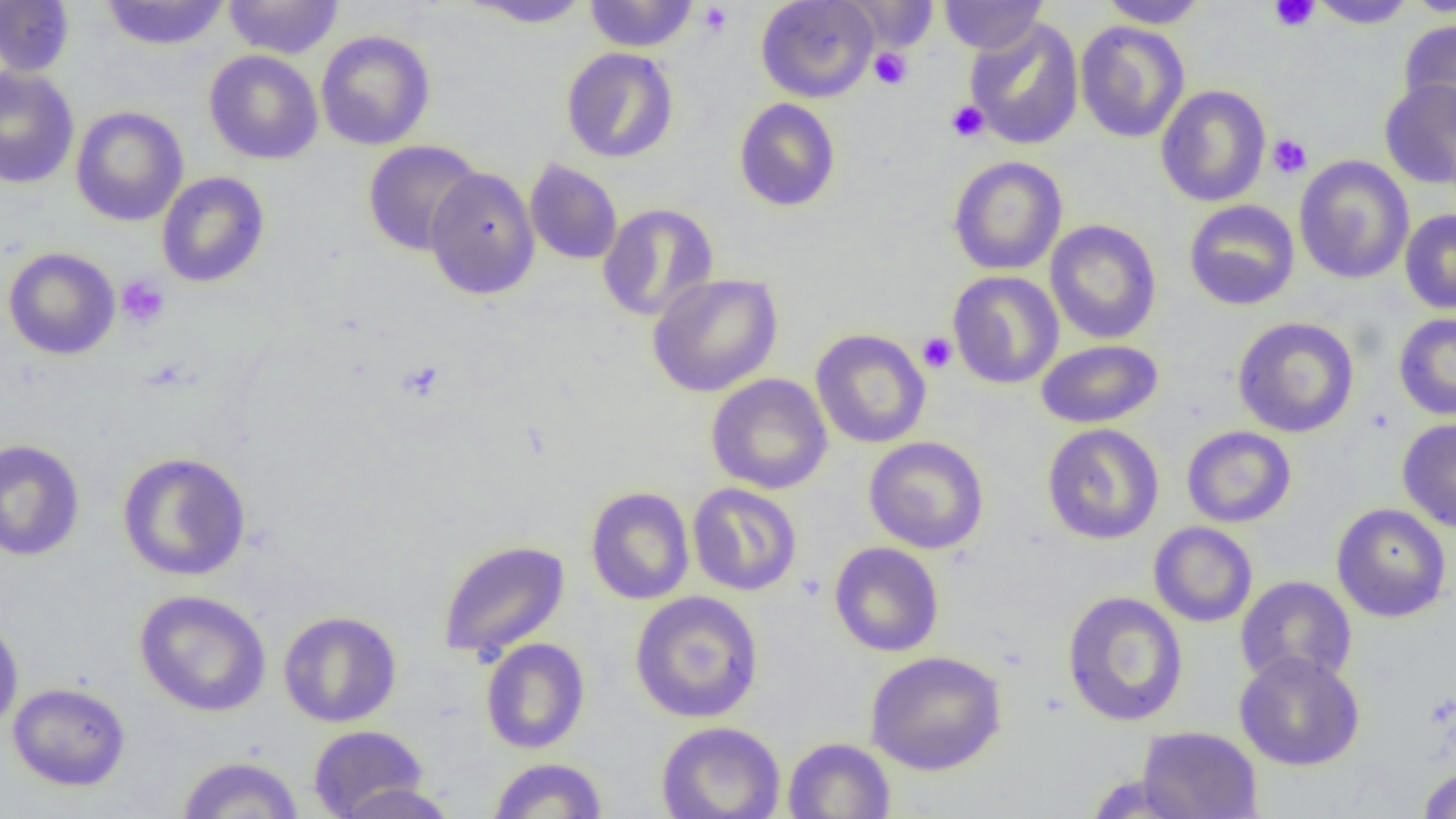 Approximate bounding boxes as named x1/y1/x2/y2 corners in pixels. Uninfected red blood cell locations: (x1=223, y1=0, x2=343, y2=59), (x1=461, y1=0, x2=594, y2=29), (x1=584, y1=0, x2=699, y2=52), (x1=756, y1=0, x2=879, y2=103), (x1=841, y1=0, x2=939, y2=51), (x1=939, y1=0, x2=1048, y2=55), (x1=1097, y1=0, x2=1209, y2=28), (x1=1309, y1=0, x2=1417, y2=29), (x1=1400, y1=0, x2=1456, y2=17), (x1=0, y1=1, x2=75, y2=78), (x1=99, y1=1, x2=231, y2=50), (x1=964, y1=17, x2=1084, y2=150), (x1=1398, y1=18, x2=1456, y2=130), (x1=1075, y1=20, x2=1190, y2=143), (x1=316, y1=30, x2=435, y2=150), (x1=561, y1=47, x2=678, y2=163), (x1=204, y1=50, x2=323, y2=164), (x1=0, y1=67, x2=79, y2=189), (x1=1379, y1=79, x2=1456, y2=190), (x1=1155, y1=85, x2=1270, y2=207), (x1=733, y1=98, x2=841, y2=212), (x1=70, y1=105, x2=188, y2=226), (x1=363, y1=140, x2=483, y2=256), (x1=1294, y1=155, x2=1414, y2=285), (x1=948, y1=156, x2=1068, y2=275), (x1=525, y1=159, x2=623, y2=265), (x1=424, y1=167, x2=540, y2=299), (x1=156, y1=172, x2=270, y2=288), (x1=1183, y1=200, x2=1300, y2=311), (x1=597, y1=203, x2=719, y2=322), (x1=1400, y1=209, x2=1456, y2=315), (x1=1045, y1=219, x2=1162, y2=344), (x1=3, y1=247, x2=120, y2=360), (x1=948, y1=270, x2=1064, y2=389), (x1=647, y1=273, x2=783, y2=398), (x1=1393, y1=313, x2=1456, y2=420), (x1=1232, y1=317, x2=1359, y2=437), (x1=811, y1=329, x2=932, y2=449), (x1=1035, y1=339, x2=1163, y2=429), (x1=706, y1=373, x2=833, y2=495), (x1=1397, y1=418, x2=1456, y2=533), (x1=1042, y1=423, x2=1164, y2=544), (x1=1181, y1=425, x2=1296, y2=528), (x1=864, y1=436, x2=989, y2=554), (x1=0, y1=439, x2=85, y2=561), (x1=117, y1=451, x2=252, y2=582), (x1=687, y1=483, x2=802, y2=596), (x1=585, y1=486, x2=695, y2=605), (x1=1331, y1=503, x2=1451, y2=623), (x1=1149, y1=522, x2=1258, y2=627), (x1=437, y1=540, x2=570, y2=661), (x1=829, y1=541, x2=945, y2=657), (x1=1235, y1=576, x2=1357, y2=688), (x1=134, y1=589, x2=272, y2=717), (x1=1062, y1=590, x2=1188, y2=727), (x1=629, y1=591, x2=764, y2=724), (x1=278, y1=610, x2=402, y2=728), (x1=0, y1=616, x2=24, y2=733), (x1=480, y1=637, x2=590, y2=754), (x1=865, y1=650, x2=1007, y2=775), (x1=1234, y1=650, x2=1366, y2=771), (x1=7, y1=682, x2=131, y2=791), (x1=656, y1=721, x2=785, y2=819), (x1=308, y1=724, x2=429, y2=818), (x1=1137, y1=726, x2=1263, y2=819), (x1=783, y1=737, x2=896, y2=819), (x1=176, y1=755, x2=304, y2=818), (x1=487, y1=757, x2=609, y2=818), (x1=1416, y1=764, x2=1456, y2=818), (x1=1081, y1=772, x2=1201, y2=818), (x1=332, y1=782, x2=460, y2=819). Platelet locations: (x1=1269, y1=0, x2=1319, y2=32), (x1=696, y1=2, x2=733, y2=38), (x1=869, y1=47, x2=911, y2=89), (x1=946, y1=101, x2=989, y2=142), (x1=1267, y1=134, x2=1312, y2=179), (x1=116, y1=274, x2=169, y2=328), (x1=917, y1=332, x2=957, y2=373), (x1=396, y1=361, x2=445, y2=402). Slide-level diagnosis: no evidence of blood parasites. Image is 1456×819 pixels. One field of a larger specimen. Thin blood film. Optical microscopy. 1000x magnification.